Classify this cell by malaria status.
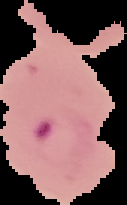

Parasitized.

Summary:
  - Image size: 127×205 pixels
  - Image type: segmented cell region with the area outside set to black
  - Preparation: thin blood film